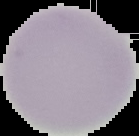
Summary:
  - Malaria status: uninfected
  - Image type: segmented cell region with the area outside set to black
  - Image size: 139×136 pixels
  - Preparation: thin blood film